Assess this cell for malaria.
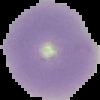
It is uninfected.

Image is 100×100 pixels. Segmented cell region on a black background. From a thin blood smear.